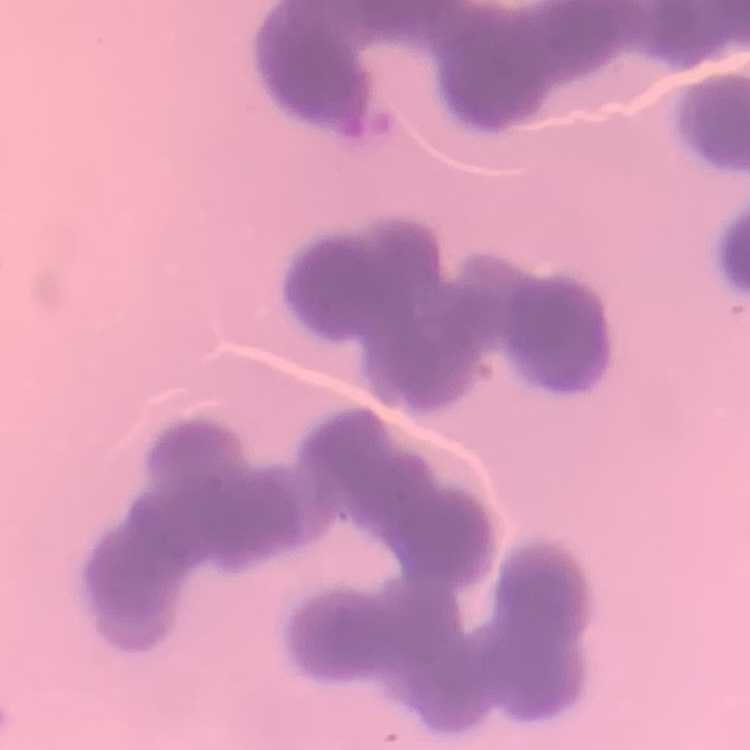

Summary:
  - Erythrocyte morphology: rouleaux formation
  - Stain: Field's or Giemsa
  - Preparation: thin blood film
  - Image type: square crop of a larger photomicrograph